State which parasite is depicted.
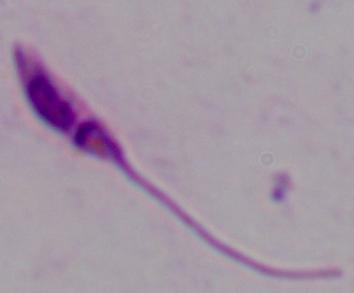
This is Leishmania.

Micrograph. Captured at 1000x magnification.